Locate every Plasmodium malariae-infected red blood cell.
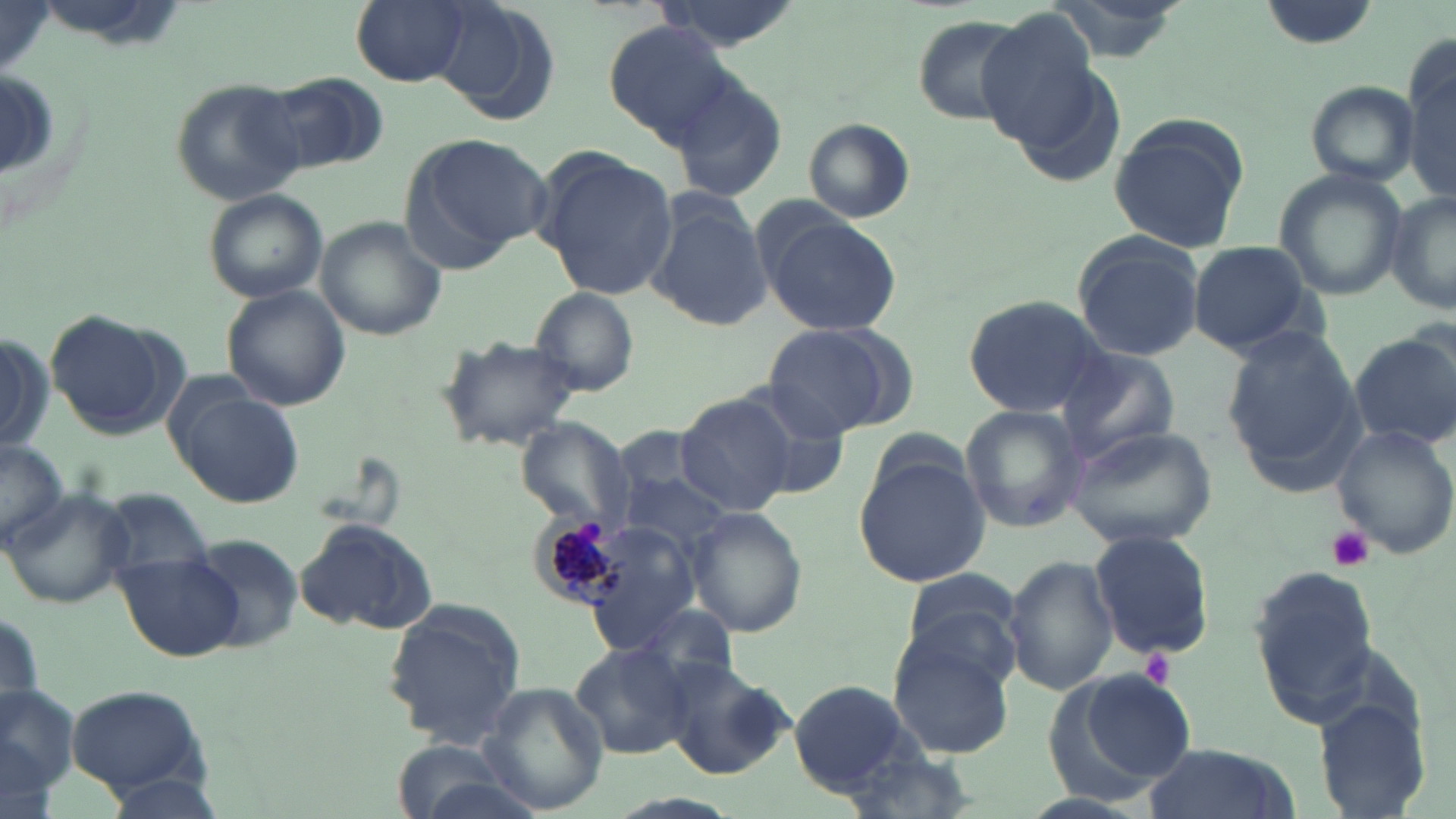
Approximate bounding boxes as [x1, y1, x2, y2] in pixels.
Plasmodium malariae-infected red blood cells: [529, 507, 634, 611].

slide_level_diagnosis: Plasmodium malariae
modality: optical microscopy
preparation: thin blood smear
field_of_view: single
platelet_locations: 'approximate bounding boxes as [x1, y1, x2, y2] in pixels: [1328, 525, 1375, 573], [1139, 650, 1177, 688]'
image_size: 1456×819 pixels
magnification: 1000x
stain: May-Grünwald-Giemsa
uninfected_red_blood_cell_locations: 'approximate bounding boxes as [x1, y1, x2, y2] in pixels: [350, 0, 472, 85], [648, 0, 809, 53], [1047, 0, 1182, 65], [1258, 0, 1382, 49], [0, 3, 54, 72], [432, 3, 563, 124], [977, 9, 1104, 152], [910, 15, 1026, 123], [601, 20, 734, 146], [1403, 39, 1455, 196], [256, 73, 389, 176], [670, 74, 790, 204], [169, 76, 306, 207], [1304, 80, 1420, 186], [1108, 112, 1248, 255], [804, 117, 915, 222], [410, 133, 558, 259], [540, 152, 680, 301], [1271, 169, 1408, 302], [203, 190, 328, 303], [649, 194, 770, 331], [1385, 194, 1456, 315], [761, 214, 902, 335], [317, 217, 447, 342], [1071, 231, 1207, 361], [1190, 241, 1314, 355], [222, 284, 351, 411], [528, 286, 641, 395], [962, 291, 1111, 419], [42, 313, 176, 438], [1222, 323, 1365, 491], [761, 324, 903, 439], [1352, 330, 1456, 450], [0, 332, 51, 452], [436, 334, 584, 451], [1057, 347, 1181, 462], [171, 385, 303, 511], [675, 391, 797, 516], [959, 404, 1088, 534], [516, 419, 630, 531], [1066, 425, 1215, 550], [1331, 425, 1455, 559], [0, 439, 69, 552], [855, 458, 991, 585], [620, 471, 733, 553], [1, 485, 130, 608], [101, 485, 215, 583], [690, 507, 808, 636], [296, 519, 442, 637], [1090, 530, 1215, 660], [186, 535, 303, 654], [117, 554, 243, 662], [1004, 555, 1120, 695], [1248, 563, 1383, 726], [899, 571, 1020, 667], [380, 599, 528, 750], [637, 603, 737, 687], [888, 630, 1016, 757], [570, 642, 696, 759], [658, 661, 792, 779], [1061, 670, 1196, 789], [0, 681, 82, 805], [788, 681, 916, 791], [477, 682, 608, 813], [67, 686, 209, 796], [1315, 693, 1434, 818], [1142, 740, 1292, 819]'